Locate every blood parasite and identify its species.
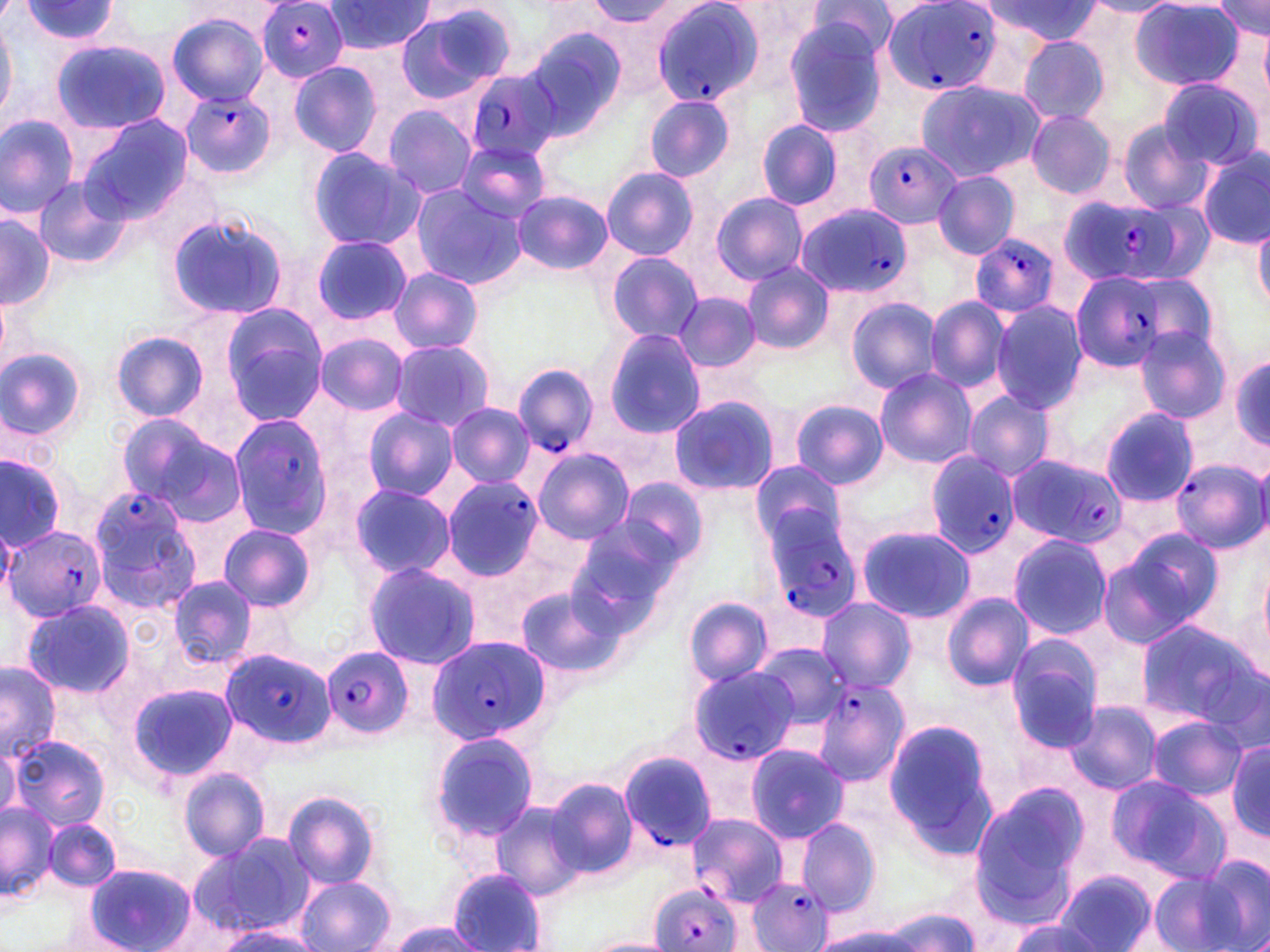
Approximate bounding boxes as (x1,y1)-(x2,y2) corner pairs in pixels.
Plasmodium falciparum-infected red blood cells: (257,0)-(348,82), (649,0)-(764,106), (881,0)-(1000,97), (468,68)-(564,164), (182,89)-(277,176), (862,141)-(961,228), (1061,194)-(1191,289), (794,203)-(913,299), (972,234)-(1060,319), (1070,270)-(1174,374), (513,365)-(598,455), (229,415)-(333,541), (926,451)-(1020,556), (1007,454)-(1124,549), (1168,457)-(1269,553), (439,476)-(543,581), (86,484)-(199,606), (758,504)-(859,624), (4,526)-(106,622), (427,637)-(548,745), (321,646)-(414,738), (222,649)-(332,747), (688,666)-(799,765), (813,675)-(911,784), (617,749)-(715,862), (688,817)-(784,905), (746,874)-(834,952), (644,888)-(737,952).
No Plasmodium ovale, Plasmodium malariae, Plasmodium vivax, Babesia divergens, or Trypanosoma brucei observed.

Uninfected red blood cell locations: (19,0)-(123,46), (1215,0)-(1269,42), (324,1)-(433,55), (588,1)-(677,25), (809,1)-(898,61), (981,1)-(1100,44), (1083,1)-(1178,16), (1129,1)-(1246,91), (395,6)-(514,103), (166,12)-(271,107), (0,15)-(15,125), (780,16)-(891,136), (525,28)-(626,137), (1260,29)-(1269,97), (1018,33)-(1111,125), (52,39)-(170,134), (288,60)-(382,157), (1157,76)-(1265,170), (914,79)-(1042,183), (643,94)-(736,183), (381,105)-(478,199), (1024,110)-(1117,199), (1,114)-(79,217), (76,115)-(194,220), (757,120)-(847,210), (1116,120)-(1214,215), (456,139)-(551,222), (306,146)-(425,252), (1198,150)-(1270,250), (601,168)-(699,260), (933,170)-(1020,260), (34,178)-(130,269), (408,184)-(526,289), (514,191)-(612,274), (711,192)-(807,286), (166,211)-(290,321), (0,216)-(54,310), (1252,217)-(1270,314), (310,236)-(413,326), (606,251)-(704,345), (741,262)-(833,354), (389,268)-(483,355), (1129,271)-(1219,359), (0,288)-(10,366), (675,292)-(760,371), (845,296)-(942,394), (925,297)-(1011,393), (990,302)-(1087,413), (220,308)-(326,422), (1133,325)-(1232,425), (604,329)-(705,437), (111,330)-(209,423), (314,332)-(410,415), (388,340)-(495,431), (0,346)-(87,442), (1229,350)-(1270,450), (874,368)-(978,468), (963,391)-(1054,480), (667,395)-(779,498), (789,400)-(889,489), (445,404)-(535,487), (363,408)-(458,501), (1101,408)-(1201,508), (116,413)-(240,518), (533,448)-(634,543), (0,456)-(66,549), (749,460)-(846,548), (615,477)-(707,571), (347,483)-(455,579), (217,524)-(316,612), (856,524)-(973,623), (566,525)-(679,633), (1101,533)-(1220,644), (1008,534)-(1112,640), (1255,555)-(1270,664), (361,560)-(482,671), (167,576)-(258,669), (514,583)-(625,679), (942,593)-(1035,691), (20,598)-(137,699), (684,598)-(775,687), (819,598)-(916,690), (1134,618)-(1265,731), (1004,635)-(1108,749), (753,643)-(848,731), (1,664)-(59,761), (128,683)-(237,783), (1065,699)-(1165,795), (1145,715)-(1248,801), (884,718)-(1003,854), (430,730)-(540,845), (8,734)-(110,832), (0,741)-(20,823), (1228,742)-(1269,839), (745,744)-(850,842), (177,766)-(271,863), (1103,775)-(1228,880), (546,778)-(638,878), (968,783)-(1092,924), (282,789)-(381,890), (491,800)-(587,899), (1,801)-(59,901), (45,818)-(120,893), (794,818)-(883,915), (188,833)-(309,937), (1199,854)-(1269,952), (85,864)-(196,952), (448,869)-(548,951), (1056,869)-(1156,951), (1149,869)-(1247,952), (295,875)-(397,952), (878,907)-(980,950), (194,920)-(317,951), (1006,920)-(1105,952), (385,921)-(491,951), (811,927)-(920,952), (581,937)-(678,952). Slide-level diagnosis: Plasmodium falciparum. Image is 1270×952 pixels. May-Grünwald-Giemsa stain. One field of a larger specimen. Captured at 1000x magnification. Thin blood film. Light microscopy.